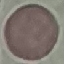

malaria status = uninfected
image type = cell patch, automatically extracted from a larger field of view and resized to 64 × 64 pixels
stain = Giemsa
preparation = thin blood film
capture = smartphone through the microscope eyepiece